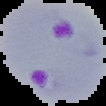
Image is 106×106 pixels. The area outside the segmented cell region is set to black. From a thin blood smear. Result: Plasmodium parasites detected.